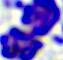
Summary:
  - Magnification: 400x
  - Identification: white blood cell
  - Modality: micrograph